Report the malaria status of this cell.
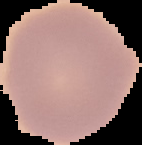

It is uninfected.

Summary:
  - Image size: 142×145 pixels
  - Image type: segmented cell region on a black background
  - Preparation: thin blood film